Classify this cell by malaria status.
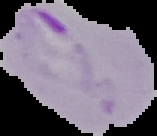
Parasitized.

image type = cell region segmented out of the field of view; surrounding area masked to black
preparation = thin blood film
image size = 157×136 pixels